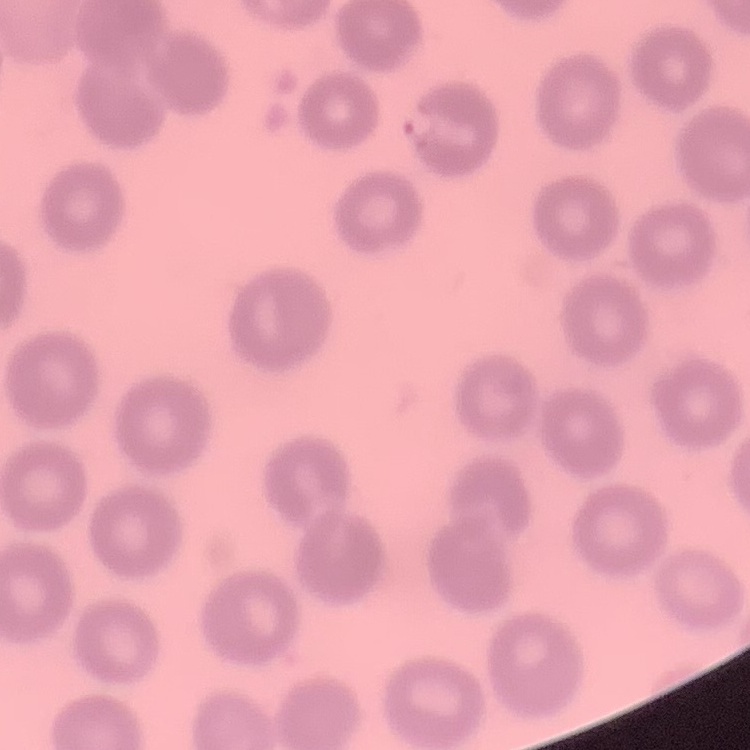

red_blood_cell_morphology: no rouleaux formation
preparation: thin blood smear
image_type: one tile cut from a larger photomicrograph
stain: Field's or Giemsa